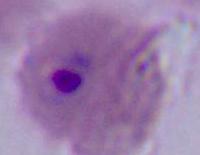

modality: photomicrograph
magnification: 400x or 1000x
identification: Plasmodium